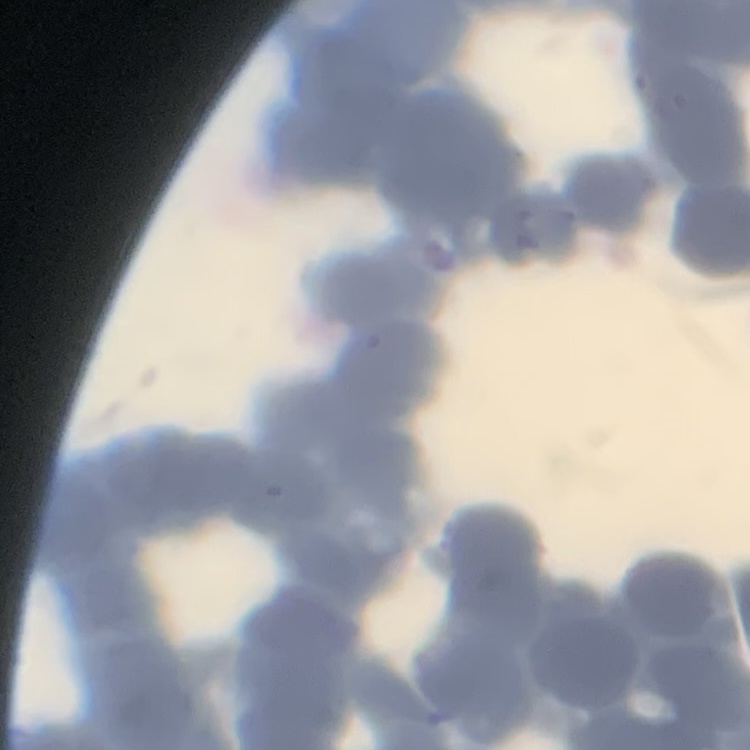 The red blood cells show rouleaux formation. One tile cut from a larger photomicrograph. Thin blood smear. Field's or Giemsa stain.